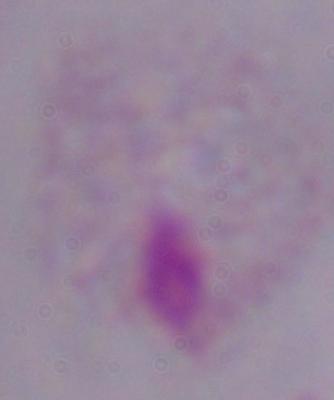

identification = trichomonad
magnification = 1000x
modality = photomicrograph